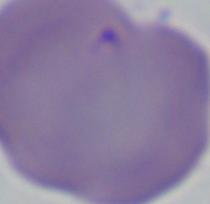 Captured at 1000x magnification. Micrograph. A Babesia parasite is shown.